Locate and identify every blood parasite.
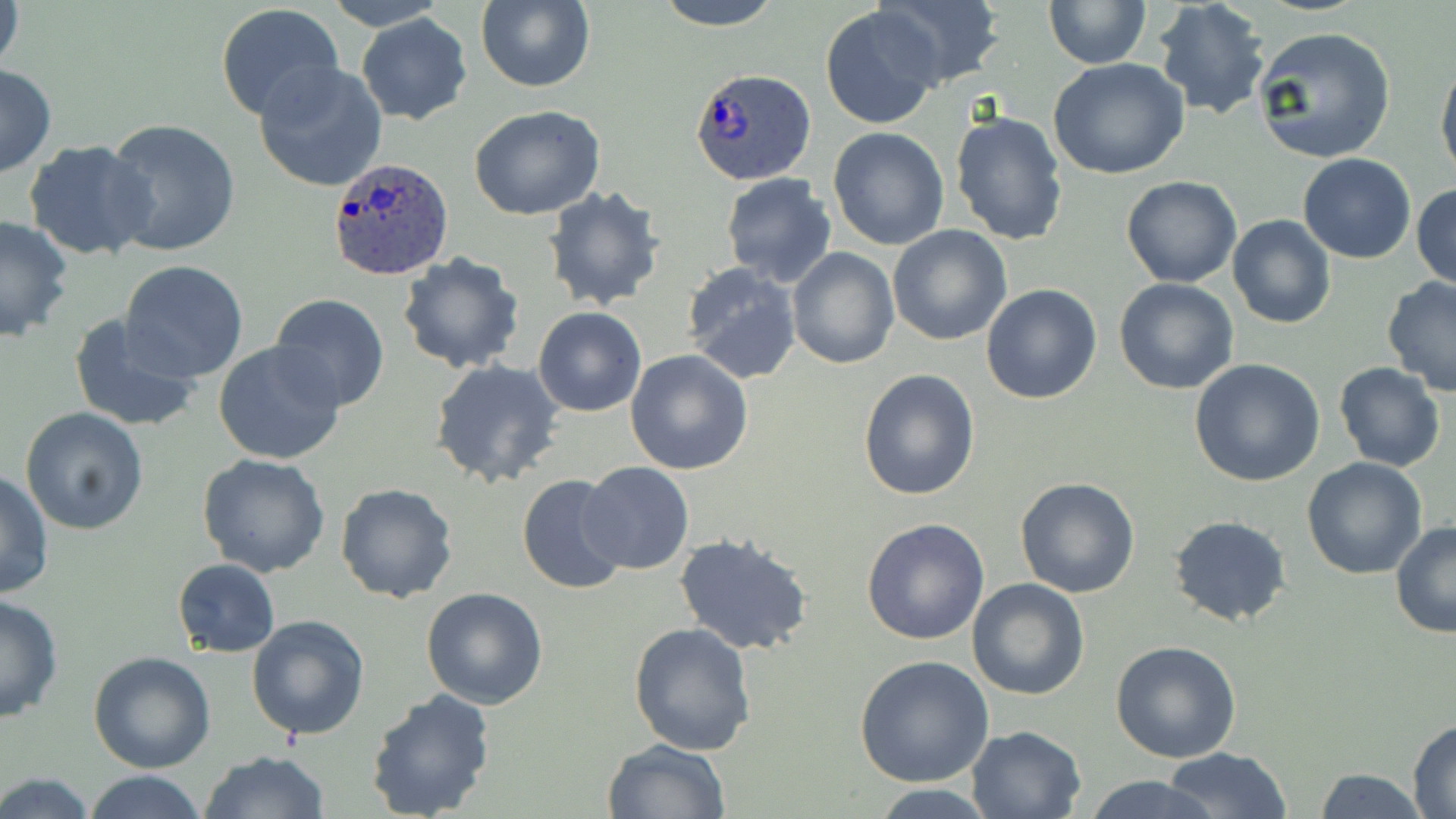
Approximate bounding boxes as (x1, y1, x2, y2) in pixels.
Plasmodium ovale-infected red blood cells: (694, 72, 819, 188), (329, 157, 455, 282).
No Plasmodium falciparum, Plasmodium malariae, Plasmodium vivax, Babesia divergens, or Trypanosoma brucei observed.

Summary:
  - Uninfected red blood cell locations: (1, 0, 26, 82), (318, 0, 454, 29), (653, 0, 785, 29), (877, 0, 1002, 90), (1044, 0, 1149, 69), (1153, 0, 1272, 121), (475, 1, 595, 92), (820, 4, 945, 129), (215, 5, 346, 126), (357, 13, 472, 125), (1252, 25, 1396, 162), (1437, 52, 1456, 186), (1047, 58, 1191, 180), (254, 63, 387, 193), (0, 64, 56, 179), (468, 104, 606, 219), (950, 109, 1068, 247), (102, 119, 241, 258), (827, 128, 948, 249), (24, 138, 157, 261), (1297, 154, 1416, 263), (719, 172, 837, 286), (1121, 175, 1243, 288), (1412, 183, 1456, 291), (541, 184, 667, 312), (1227, 214, 1336, 329), (0, 215, 73, 340), (888, 225, 1013, 346), (786, 246, 899, 367), (394, 252, 528, 375), (120, 260, 249, 381), (681, 261, 804, 383), (1382, 277, 1456, 394), (1113, 278, 1239, 395), (981, 283, 1104, 404), (269, 293, 391, 413), (533, 306, 647, 417), (68, 313, 202, 433), (214, 341, 346, 465), (624, 348, 754, 477), (429, 359, 564, 488), (1191, 359, 1326, 487), (1334, 361, 1446, 472), (857, 368, 980, 500), (20, 406, 150, 534), (198, 453, 330, 576), (1302, 456, 1427, 579), (578, 461, 694, 575), (0, 469, 53, 600), (516, 472, 633, 597), (1014, 477, 1141, 598), (334, 482, 457, 604), (1168, 515, 1292, 627), (861, 517, 990, 646), (1390, 521, 1456, 638), (674, 533, 813, 654), (171, 558, 280, 658), (966, 578, 1089, 700), (421, 587, 548, 709), (0, 592, 63, 723), (246, 613, 372, 739), (628, 622, 758, 755), (1110, 640, 1242, 762), (89, 652, 216, 773), (856, 656, 995, 788), (363, 687, 497, 819), (1407, 719, 1456, 816), (967, 725, 1087, 818), (601, 739, 730, 819), (1163, 746, 1292, 819), (201, 750, 330, 819), (1309, 766, 1427, 819), (82, 771, 211, 819), (0, 772, 98, 818), (1081, 774, 1219, 819), (868, 785, 1002, 817)
  - Slide-level diagnosis: Plasmodium ovale
  - Stain: May-Grünwald-Giemsa
  - Preparation: thin blood film
  - Magnification: 1000x
  - Modality: optical microscopy
  - Field of view: one of a larger specimen
  - Image size: 1456×819 pixels